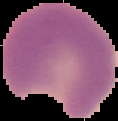
Summary:
  - Preparation: thin blood film
  - Result: Plasmodium parasites detected
  - Image size: 118×121 pixels
  - Image type: segmented cell region with the area outside set to black